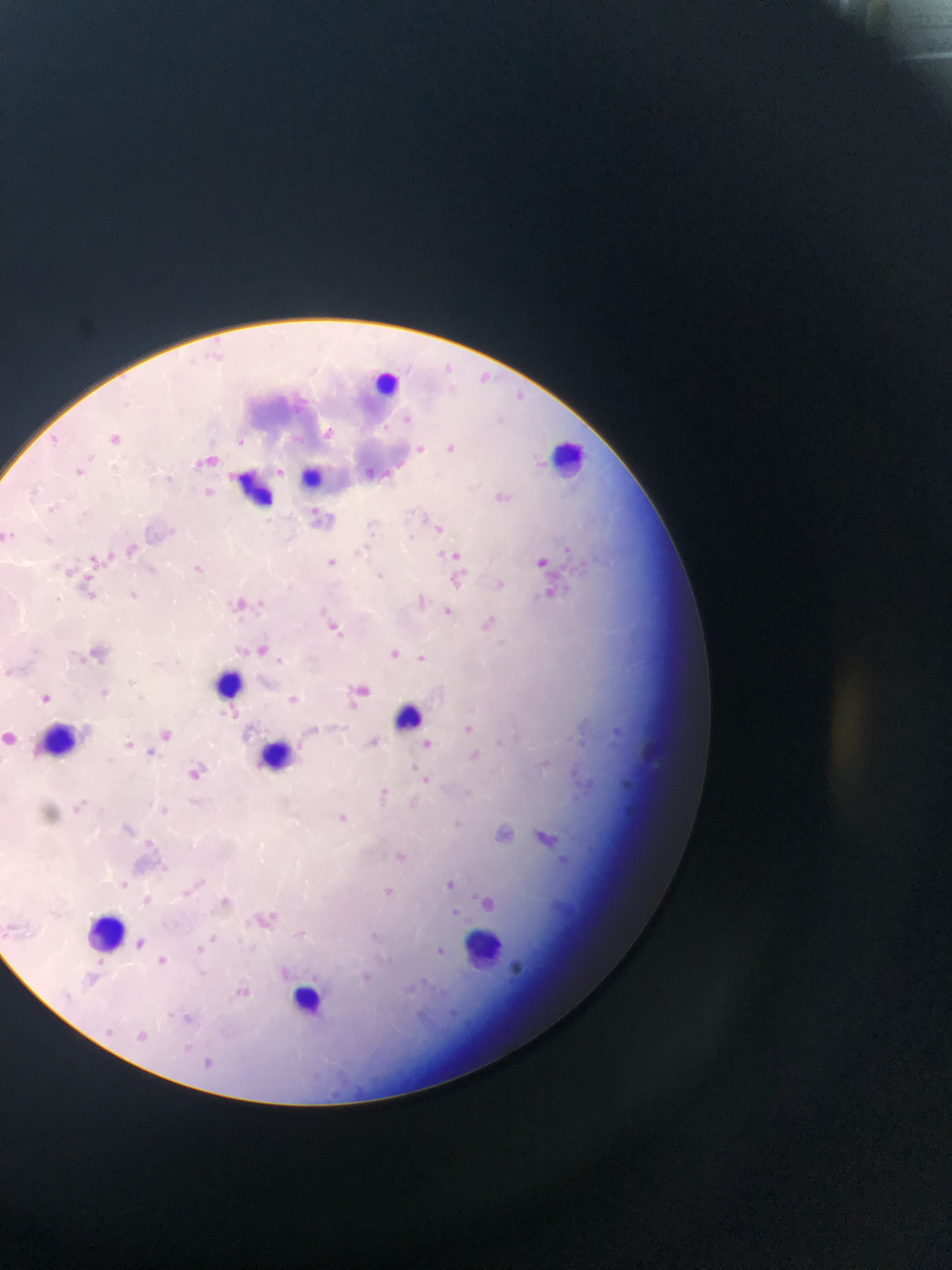
malaria parasite locations = approximate bounding boxes as {left, top, right, bottom} in pixels: {437, 363, 452, 375}, {478, 371, 500, 387}, {516, 390, 530, 403}, {400, 411, 420, 427}, {383, 421, 392, 432}, {315, 425, 342, 440}, {109, 432, 131, 453}, {45, 435, 61, 447}, {236, 437, 251, 452}, {416, 442, 427, 456}, {446, 445, 467, 459}, {191, 458, 205, 472}, {394, 461, 405, 470}, {277, 463, 285, 479}, {78, 472, 96, 489}, {497, 492, 514, 509}, {307, 504, 321, 515}, {432, 523, 454, 539}, {164, 525, 180, 541}, {365, 530, 380, 539}, {409, 532, 424, 545}, {104, 541, 123, 561}, {565, 544, 575, 555}, {129, 547, 139, 553}, {353, 549, 366, 563}, {451, 553, 467, 562}, {329, 557, 344, 574}, {535, 557, 551, 569}, {189, 559, 208, 577}, {561, 560, 585, 574}, {84, 568, 97, 583}, {376, 572, 386, 582}, {495, 575, 509, 591}, {452, 576, 466, 593}, {553, 583, 564, 591}, {563, 583, 575, 592}, {541, 586, 555, 597}, {86, 591, 98, 602}, {128, 593, 142, 610}, {252, 596, 267, 613}, {314, 600, 335, 614}, {439, 608, 456, 626}, {487, 609, 502, 629}, {233, 616, 251, 626}, {332, 627, 347, 639}, {385, 646, 403, 660}, {418, 651, 427, 663}, {272, 653, 287, 661}, {40, 693, 51, 704}, {217, 707, 228, 726}, {464, 721, 474, 738}, {368, 733, 378, 748}, {496, 736, 512, 749}, {612, 736, 622, 749}, {125, 739, 136, 752}, {423, 739, 432, 748}, {147, 745, 157, 756}, {542, 758, 557, 770}, {409, 760, 421, 774}, {189, 765, 210, 780}, {423, 777, 431, 785}, {622, 779, 636, 792}, {378, 784, 394, 793}, {572, 790, 587, 805}, {80, 796, 92, 805}, {69, 803, 85, 814}, {157, 805, 171, 813}, {336, 815, 354, 829}, {453, 817, 475, 836}, {150, 844, 161, 860}, {393, 847, 408, 864}, {558, 855, 569, 869}, {159, 863, 171, 876}, {439, 876, 462, 889}, {195, 877, 210, 894}, {120, 880, 132, 889}, {385, 887, 394, 896}, {470, 890, 482, 903}, {220, 892, 233, 908}, {453, 908, 463, 918}, {264, 915, 291, 931}, {296, 930, 306, 938}, {209, 932, 221, 945}, {437, 940, 447, 957}, {195, 945, 205, 957}, {95, 955, 108, 968}, {157, 955, 167, 965}, {280, 963, 292, 988}, {198, 967, 208, 977}, {235, 984, 258, 1009}, {167, 1006, 177, 1019}, {179, 1011, 191, 1024}, {188, 1043, 197, 1048}, {204, 1058, 213, 1069}
image size = 952×1270 pixels
field of view = single
preparation = thin blood film
leukocyte locations = approximate bounding boxes as {left, top, right, bottom} in pixels: {371, 361, 403, 401}, {545, 440, 597, 484}, {301, 462, 319, 484}, {226, 468, 262, 512}, {205, 671, 251, 705}, {392, 699, 422, 731}, {46, 709, 93, 747}, {263, 739, 304, 777}, {82, 904, 140, 953}, {468, 929, 499, 972}, {291, 981, 341, 1008}
country = Ghana
capture = mobile-phone photograph through a microscope